Identify the parasite.
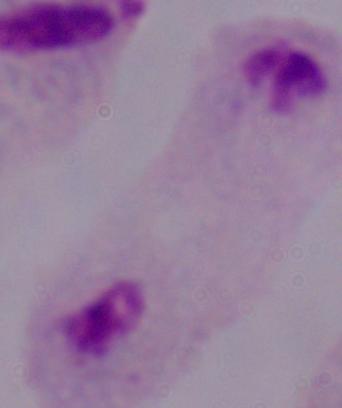
This is a trichomonad.

1000x magnification. Photomicrograph.